Assess the morphology of the red blood cells.
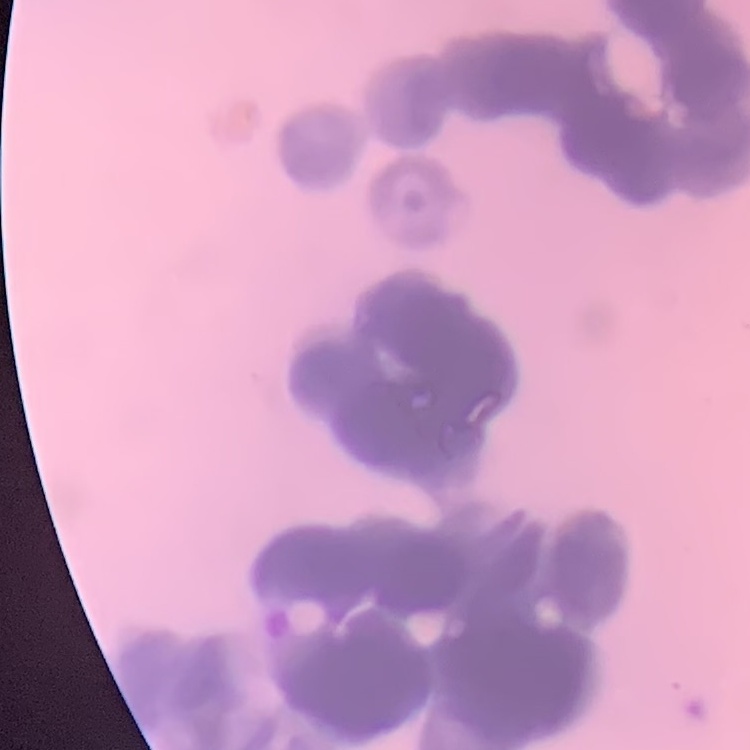

Rouleaux formation.

Summary:
  - Stain: Field's or Giemsa
  - Image type: one tile cut from a larger photomicrograph
  - Preparation: thin blood film